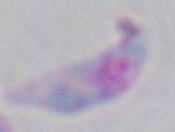

Summary:
  - Magnification: 1000x
  - Modality: photomicrograph
  - Identification: Toxoplasma gondii